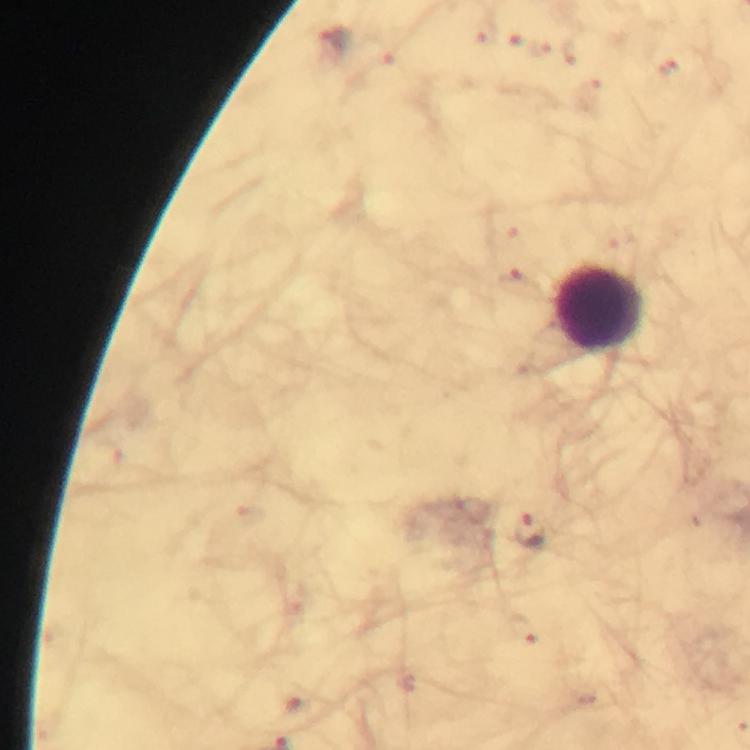

Approximate centers as {x, y} in pixels.
Summary:
  - Leukocyte locations: {600, 308}
  - Malaria parasite locations: {335, 39}, {529, 532}
  - Immersion oil: used
  - Stain: Giemsa
  - Context: from a malaria diagnostic workup
  - Preparation: thick smear
  - Image size: 750×750 pixels
  - Cropped from: a single field of view
  - Magnification: 100x
  - Capture: smartphone photograph through a microscope